Identify the blood parasite species.
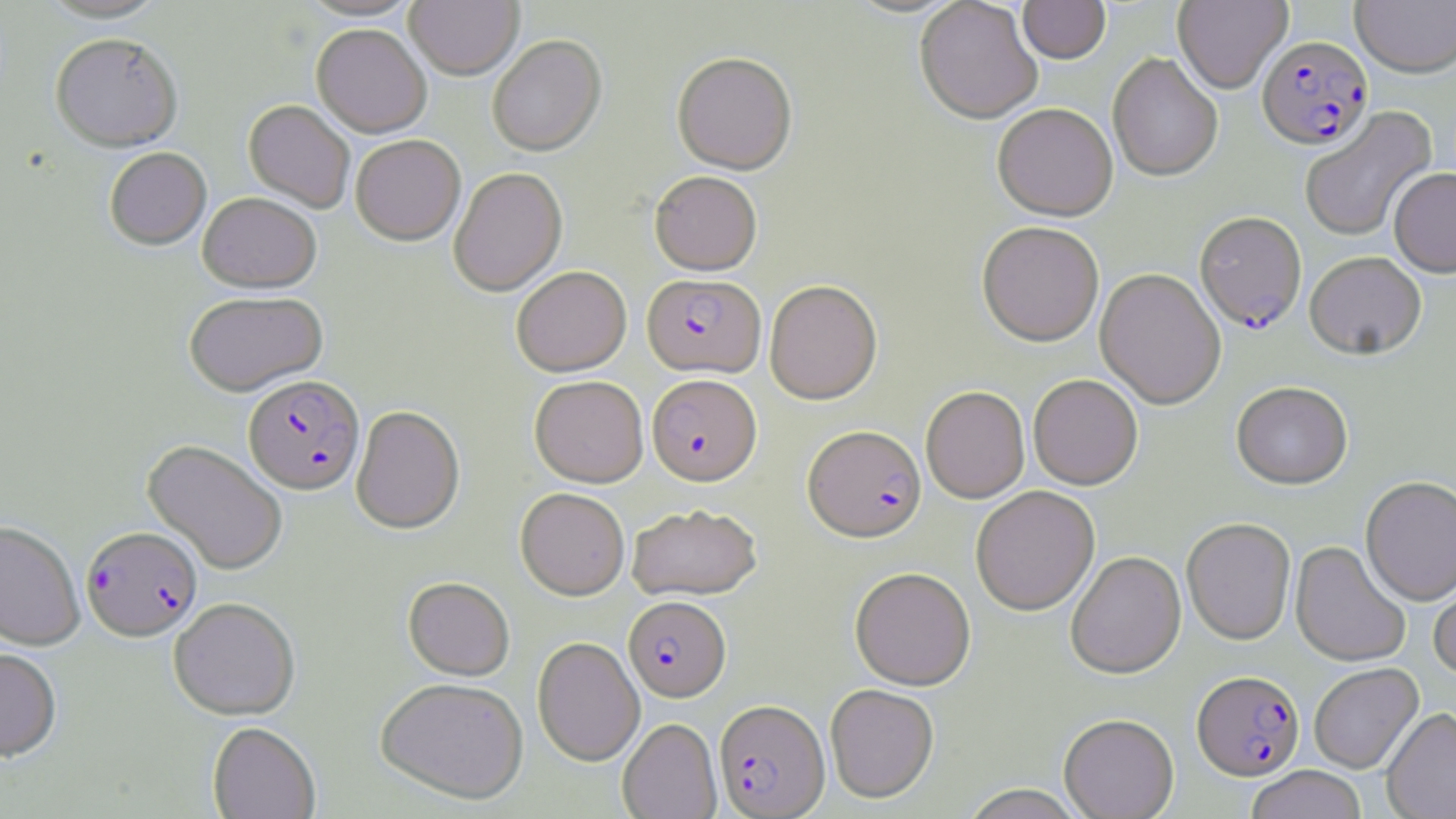

Plasmodium falciparum.

Summary:
  - Coordinate format: approximate bounding boxes as (x1, y1, x2, y2) in pixels
  - Uninfected red blood cell locations: (39, 0, 168, 22), (299, 0, 422, 21), (845, 0, 965, 19), (1017, 0, 1111, 67), (1173, 0, 1292, 95), (1351, 0, 1456, 80), (405, 1, 524, 80), (914, 1, 1042, 128), (312, 25, 432, 139), (50, 33, 183, 152), (487, 37, 607, 158), (672, 55, 798, 177), (1108, 55, 1223, 184), (243, 101, 355, 214), (992, 106, 1117, 225), (1300, 106, 1439, 243), (350, 136, 466, 247), (104, 148, 212, 251), (448, 168, 567, 298), (1389, 170, 1456, 281), (649, 172, 762, 277), (198, 193, 322, 293), (977, 224, 1104, 349), (1305, 254, 1426, 363), (512, 266, 631, 377), (1094, 269, 1226, 411), (765, 282, 883, 406), (184, 292, 328, 397), (1028, 375, 1143, 490), (530, 376, 648, 488), (1231, 383, 1353, 492), (920, 387, 1029, 504), (351, 406, 465, 535), (143, 439, 288, 575), (1360, 478, 1456, 609), (971, 487, 1099, 617), (516, 488, 630, 600), (627, 504, 762, 602), (1181, 519, 1296, 647), (0, 520, 85, 651), (1290, 542, 1410, 669), (1066, 553, 1186, 681), (1430, 567, 1456, 682), (850, 568, 976, 691), (403, 577, 515, 681), (168, 598, 300, 720), (532, 637, 644, 766), (0, 648, 62, 763), (1309, 664, 1425, 776), (375, 678, 529, 806), (825, 685, 939, 805), (1382, 708, 1456, 819), (1059, 716, 1179, 819), (618, 718, 722, 819), (207, 722, 320, 819), (1246, 767, 1366, 819), (959, 785, 1087, 819)
  - Plasmodium falciparum-infected red blood cell locations: (1257, 38, 1374, 153), (1193, 214, 1307, 336), (642, 274, 765, 379), (243, 375, 364, 495), (646, 376, 762, 488), (803, 426, 927, 544), (81, 527, 203, 642), (623, 597, 730, 703), (1191, 672, 1305, 782), (715, 700, 830, 818)
  - Image size: 1456×819 pixels
  - Field of view: one of a larger specimen
  - Preparation: thin blood film
  - Modality: optical microscopy
  - Stain: May-Grünwald-Giemsa
  - Magnification: 1000x